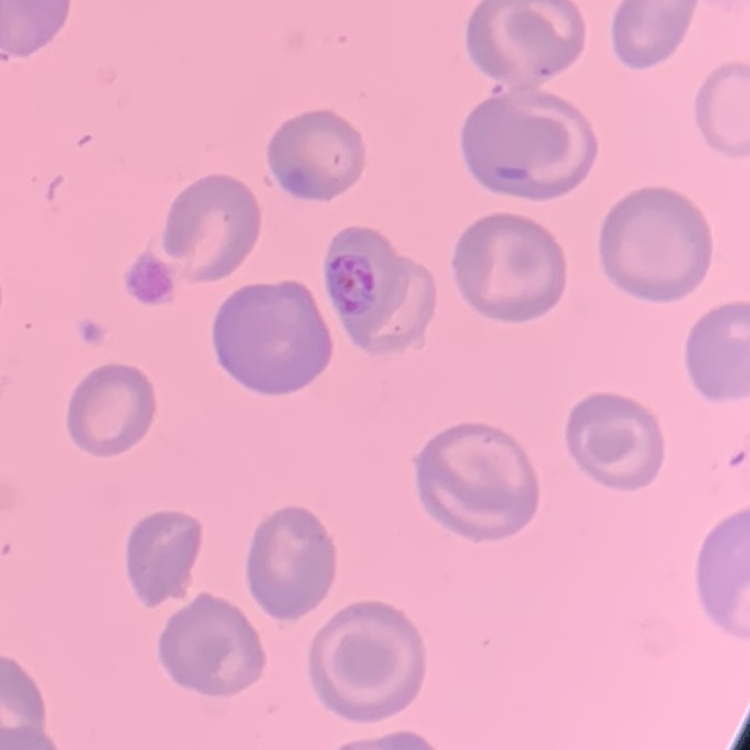

The erythrocytes exhibit no rouleaux formation. Stained with either Field's or Giemsa. Thin blood film. Square crop of a larger photomicrograph.